Report the malaria status of this cell.
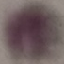

Uninfected.

Summary:
  - Preparation: thin blood film
  - Image type: automatically extracted cell patch, resized to 64 × 64 pixels
  - Capture: smartphone through the microscope eyepiece
  - Stain: Giemsa